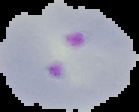

preparation: thin blood smear
image_type: segmented cell region with the area outside set to black
image_size: 139×112 pixels
malaria_status: parasitized